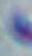

identification = Toxoplasma gondii
modality = photomicrograph
magnification = 1000x